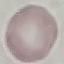

malaria status = uninfected
stain = Giemsa
image type = automatically extracted cell patch, resized to 64 × 64 pixels
preparation = thin blood smear
capture = smartphone camera at the microscope eyepiece